Assess this cell for malaria.
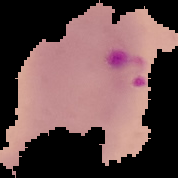
Parasitized.

From a thin blood film. Image is 178×178 pixels. The area outside the segmented cell region is set to black.